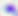

identification = Toxoplasma gondii
magnification = 400x
modality = micrograph